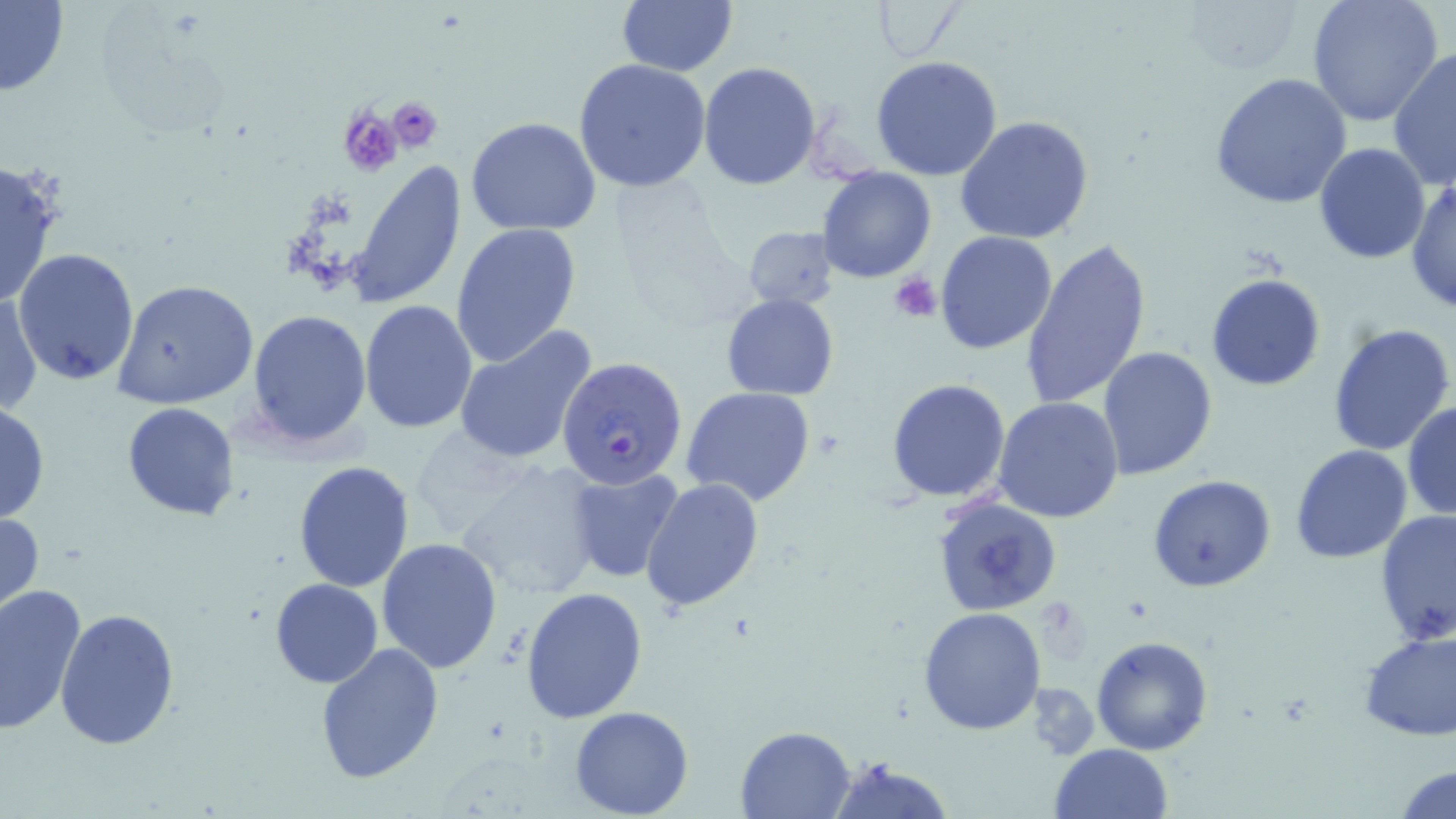
Summary:
  - Coordinate format: approximate bounding boxes as (x1,y1)-(x2,y2) corner pairs in pixels
  - Plasmodium falciparum-infected red blood cell locations: (558,356)-(688,489)
  - Platelet locations: (386,94)-(443,154), (339,106)-(406,178), (890,271)-(941,323)
  - Uninfected red blood cell locations: (1183,0)-(1305,78), (1305,0)-(1443,126), (616,1)-(737,77), (871,1)-(966,64), (0,2)-(70,96), (1388,46)-(1456,191), (870,56)-(1003,180), (574,58)-(711,193), (698,62)-(821,191), (1210,73)-(1354,211), (466,116)-(601,236), (956,116)-(1095,243), (1314,142)-(1430,264), (0,158)-(63,309), (345,161)-(468,310), (817,165)-(937,283), (1408,178)-(1455,310), (450,222)-(581,368), (742,224)-(841,311), (935,230)-(1057,355), (1020,235)-(1154,410), (13,248)-(140,384), (1206,273)-(1325,391), (113,278)-(260,409), (1,290)-(43,419), (721,294)-(839,401), (359,300)-(478,434), (245,309)-(372,451), (1328,321)-(1455,456), (454,327)-(597,465), (1098,347)-(1218,481), (886,377)-(1012,503), (681,386)-(815,506), (994,397)-(1125,524), (0,401)-(49,526), (121,402)-(239,520), (1402,403)-(1456,523), (1290,445)-(1412,564), (455,458)-(607,601), (293,462)-(413,592), (566,466)-(683,583), (1149,474)-(1275,591), (640,476)-(765,611), (932,493)-(1064,619), (0,509)-(46,618), (1374,510)-(1455,647), (376,538)-(504,673), (269,578)-(383,687), (0,583)-(88,737), (521,587)-(648,725), (54,606)-(181,749), (917,606)-(1045,736), (1358,629)-(1456,741), (1090,635)-(1213,755), (315,641)-(443,783), (569,706)-(694,818), (735,724)-(857,817), (1050,743)-(1173,819), (824,757)-(953,819), (1393,763)-(1456,818)
  - Slide-level diagnosis: Plasmodium falciparum
  - Image size: 1456×819 pixels
  - Modality: light microscopy
  - Magnification: 1000x
  - Preparation: thin blood smear
  - Field of view: single
  - Stain: May-Grünwald-Giemsa